Locate every Plasmodium parasite.
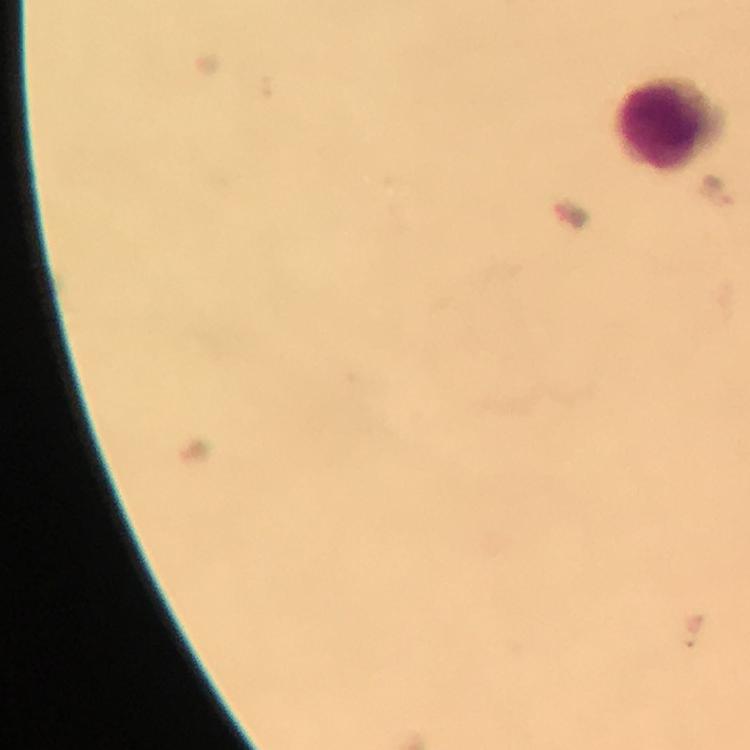

No Plasmodium parasites detected.

Approximate object centers, in pixels from the top-left corner. Leukocyte locations: (x=661, y=124). Thick smear. From a diagnostic examination for malaria. A crop from one field of view. Image is 750×750 pixels. Giemsa-stained preparation. Immersion oil applied. 100x magnification. Photographed with a smartphone mounted on the microscope.